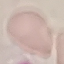
malaria status = uninfected
preparation = thin blood film
stain = Giemsa
image type = automatically extracted cell patch, resized to 64 × 64 pixels
capture = smartphone camera at the microscope eyepiece